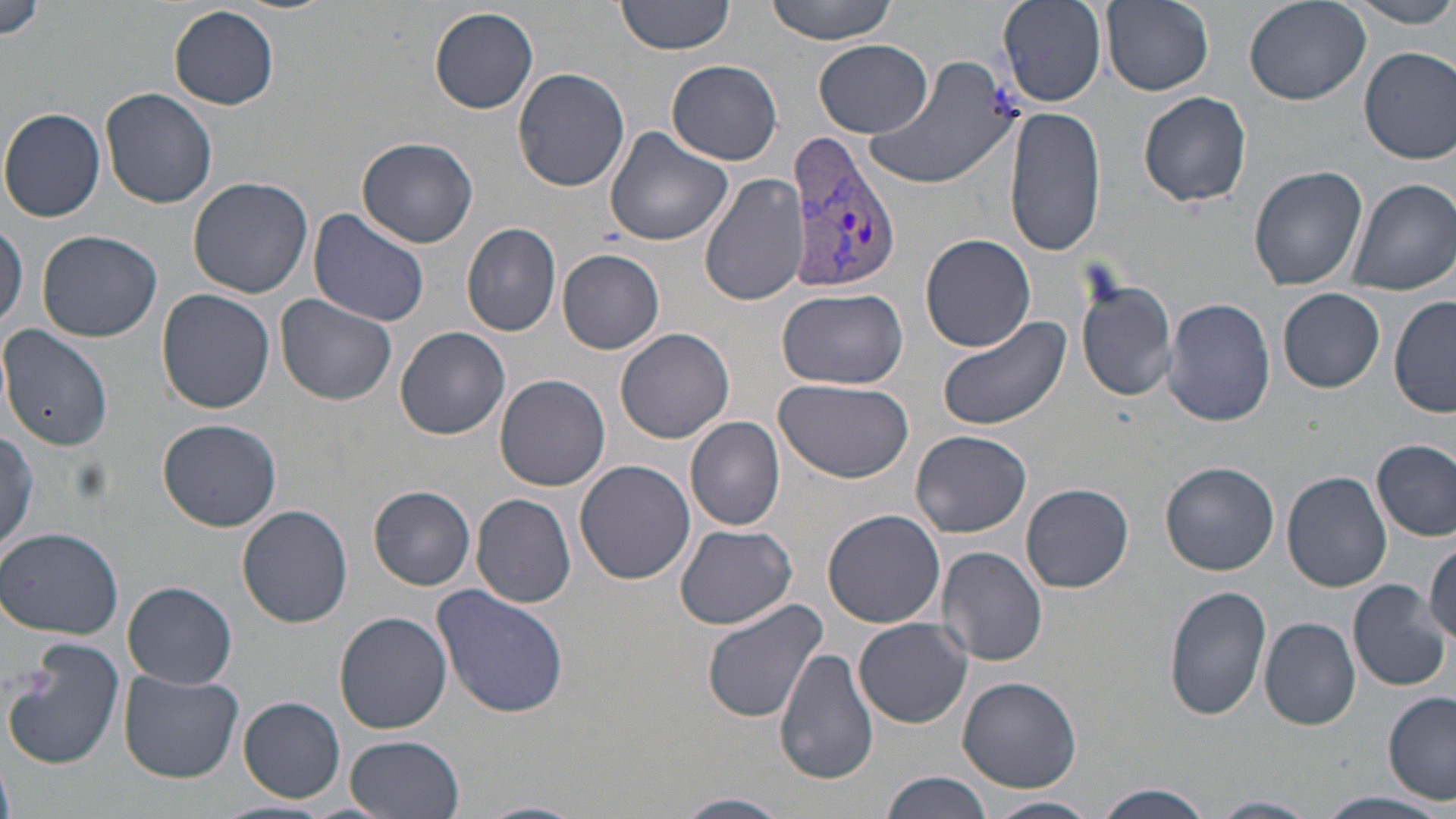

Summary:
  - Coordinate format: approximate bounding boxes as named x1/y1/x2/y2 corners in pixels
  - Plasmodium vivax-infected red blood cell locations: (x1=782, y1=133, x2=903, y2=297)
  - Uninfected red blood cell locations: (x1=616, y1=0, x2=733, y2=56), (x1=764, y1=0, x2=899, y2=43), (x1=998, y1=0, x2=1107, y2=107), (x1=1101, y1=0, x2=1213, y2=94), (x1=1243, y1=0, x2=1370, y2=105), (x1=1347, y1=1, x2=1456, y2=27), (x1=0, y1=2, x2=48, y2=43), (x1=169, y1=5, x2=278, y2=110), (x1=429, y1=6, x2=540, y2=115), (x1=812, y1=39, x2=934, y2=138), (x1=1359, y1=47, x2=1456, y2=164), (x1=862, y1=53, x2=1024, y2=191), (x1=667, y1=60, x2=782, y2=165), (x1=514, y1=67, x2=629, y2=192), (x1=100, y1=88, x2=217, y2=210), (x1=1138, y1=92, x2=1252, y2=208), (x1=1003, y1=106, x2=1106, y2=259), (x1=0, y1=108, x2=107, y2=222), (x1=603, y1=127, x2=733, y2=246), (x1=358, y1=136, x2=477, y2=248), (x1=1249, y1=165, x2=1369, y2=291), (x1=700, y1=173, x2=808, y2=306), (x1=188, y1=176, x2=313, y2=299), (x1=1345, y1=177, x2=1456, y2=295), (x1=307, y1=209, x2=432, y2=327), (x1=0, y1=218, x2=27, y2=331), (x1=462, y1=221, x2=563, y2=336), (x1=38, y1=230, x2=165, y2=343), (x1=920, y1=234, x2=1037, y2=352), (x1=557, y1=248, x2=665, y2=353), (x1=1075, y1=271, x2=1178, y2=404), (x1=777, y1=285, x2=910, y2=390), (x1=157, y1=287, x2=275, y2=413), (x1=1279, y1=288, x2=1385, y2=393), (x1=276, y1=292, x2=399, y2=405), (x1=1163, y1=297, x2=1277, y2=428), (x1=1389, y1=297, x2=1455, y2=419), (x1=938, y1=318, x2=1070, y2=431), (x1=0, y1=325, x2=114, y2=452), (x1=393, y1=326, x2=510, y2=440), (x1=617, y1=329, x2=736, y2=444), (x1=495, y1=375, x2=611, y2=492), (x1=776, y1=379, x2=915, y2=485), (x1=685, y1=416, x2=786, y2=530), (x1=157, y1=419, x2=283, y2=532), (x1=0, y1=424, x2=41, y2=559), (x1=911, y1=431, x2=1034, y2=539), (x1=1373, y1=440, x2=1455, y2=539), (x1=575, y1=460, x2=696, y2=586), (x1=1161, y1=463, x2=1279, y2=576), (x1=1282, y1=470, x2=1392, y2=593), (x1=1022, y1=483, x2=1133, y2=593), (x1=369, y1=486, x2=475, y2=589), (x1=471, y1=493, x2=576, y2=608), (x1=238, y1=505, x2=353, y2=628), (x1=822, y1=508, x2=947, y2=628), (x1=674, y1=524, x2=801, y2=631), (x1=0, y1=527, x2=124, y2=639), (x1=1426, y1=539, x2=1456, y2=646), (x1=935, y1=546, x2=1049, y2=667), (x1=1348, y1=580, x2=1451, y2=691), (x1=123, y1=581, x2=238, y2=689), (x1=1163, y1=583, x2=1268, y2=721), (x1=432, y1=584, x2=571, y2=719), (x1=700, y1=599, x2=827, y2=726), (x1=335, y1=612, x2=452, y2=733), (x1=1260, y1=616, x2=1360, y2=730), (x1=855, y1=618, x2=973, y2=727), (x1=3, y1=642, x2=125, y2=771), (x1=776, y1=647, x2=878, y2=785), (x1=120, y1=670, x2=243, y2=782), (x1=955, y1=676, x2=1081, y2=791), (x1=1383, y1=691, x2=1456, y2=803), (x1=237, y1=696, x2=346, y2=803), (x1=345, y1=735, x2=464, y2=818), (x1=879, y1=772, x2=992, y2=819), (x1=1095, y1=784, x2=1214, y2=819), (x1=1312, y1=791, x2=1453, y2=819), (x1=671, y1=793, x2=791, y2=818), (x1=983, y1=795, x2=1099, y2=819), (x1=1208, y1=795, x2=1320, y2=818), (x1=476, y1=799, x2=588, y2=819)
  - Slide-level diagnosis: Plasmodium vivax
  - Magnification: 1000x
  - Field of view: single
  - Preparation: thin blood smear
  - Modality: optical microscopy
  - Stain: May-Grünwald-Giemsa
  - Image size: 1456×819 pixels